Name the parasite shown.
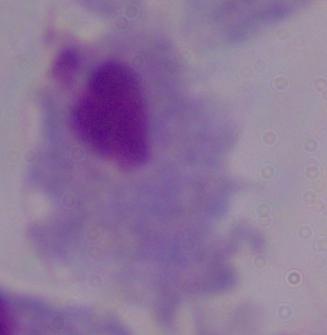

A trichomonad.

Micrograph. Captured at 1000x magnification.